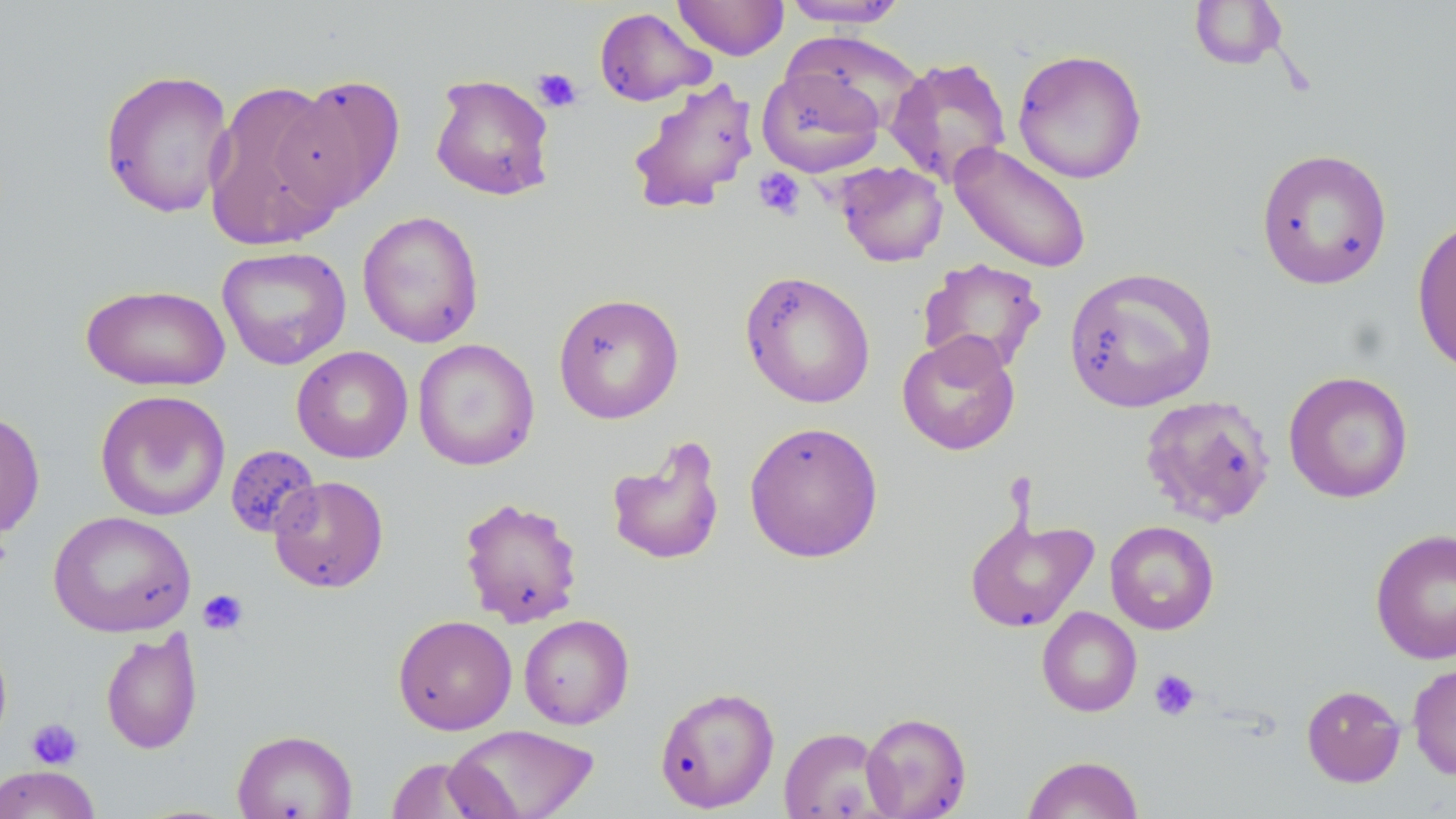
Approximate bounding boxes as [x1, y1, x2, y2] in pixels. Platelet locations: [532, 67, 583, 113], [753, 167, 806, 220], [198, 589, 249, 634], [1149, 669, 1200, 720], [26, 718, 83, 770]. Uninfected red blood cell locations: [780, 0, 910, 28], [672, 1, 789, 60], [1188, 1, 1288, 71], [594, 6, 714, 106], [785, 32, 925, 134], [1012, 48, 1148, 185], [886, 56, 1013, 188], [757, 66, 885, 177], [99, 68, 235, 218], [429, 72, 556, 201], [273, 74, 407, 213], [626, 75, 760, 216], [203, 80, 347, 251], [950, 142, 1092, 273], [1255, 148, 1393, 290], [834, 161, 948, 267], [357, 210, 484, 348], [1412, 216, 1456, 375], [216, 245, 352, 370], [917, 257, 1047, 376], [1063, 266, 1218, 413], [739, 269, 876, 409], [80, 283, 231, 391], [553, 293, 684, 424], [896, 331, 1021, 456], [413, 339, 540, 471], [292, 345, 413, 463], [1283, 370, 1414, 504], [94, 390, 231, 522], [1139, 394, 1276, 527], [0, 409, 45, 539], [743, 421, 884, 563], [605, 435, 726, 566], [224, 445, 322, 540], [268, 475, 388, 593], [458, 496, 583, 628], [47, 510, 196, 637], [964, 511, 1098, 633], [1105, 520, 1219, 635], [1369, 527, 1456, 665], [1037, 606, 1142, 717], [518, 614, 634, 729], [392, 615, 517, 735], [0, 627, 12, 754], [100, 628, 203, 755], [1407, 662, 1456, 780], [1301, 684, 1406, 787], [654, 685, 780, 813], [860, 711, 972, 818], [446, 723, 600, 819], [779, 726, 890, 818], [232, 729, 358, 819], [1022, 754, 1144, 818], [382, 757, 506, 818], [0, 765, 101, 819]. Slide-level diagnosis: negative for blood parasites. May-Grünwald-Giemsa stain. Light microscopy. One field of a larger specimen. Thin blood smear. Captured at 1000x magnification. Image is 1456×819 pixels.